Comment on the morphology of the red blood cells.
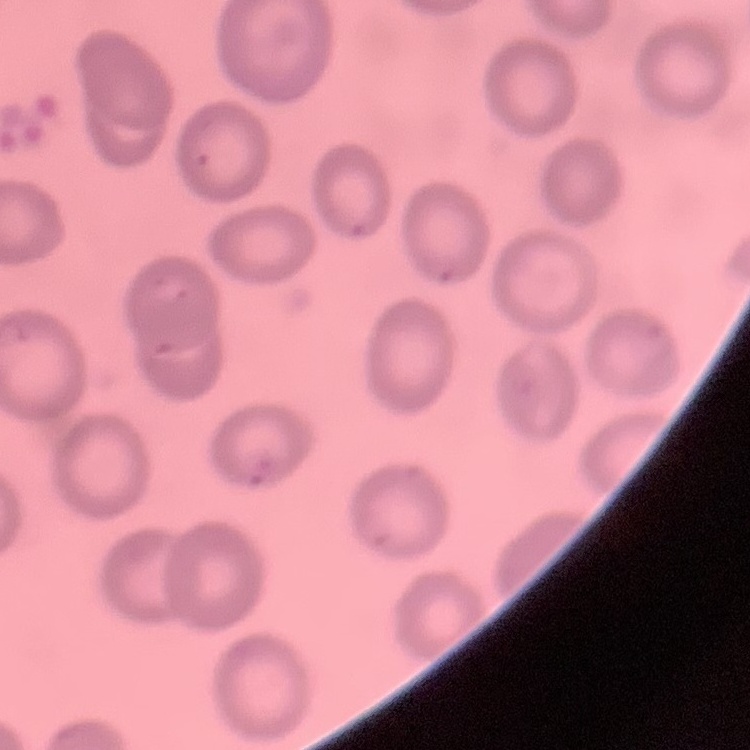

No rouleaux formation.

Summary:
  - Image type: one tile cut from a larger photomicrograph
  - Preparation: thin blood film
  - Stain: Field's or Giemsa